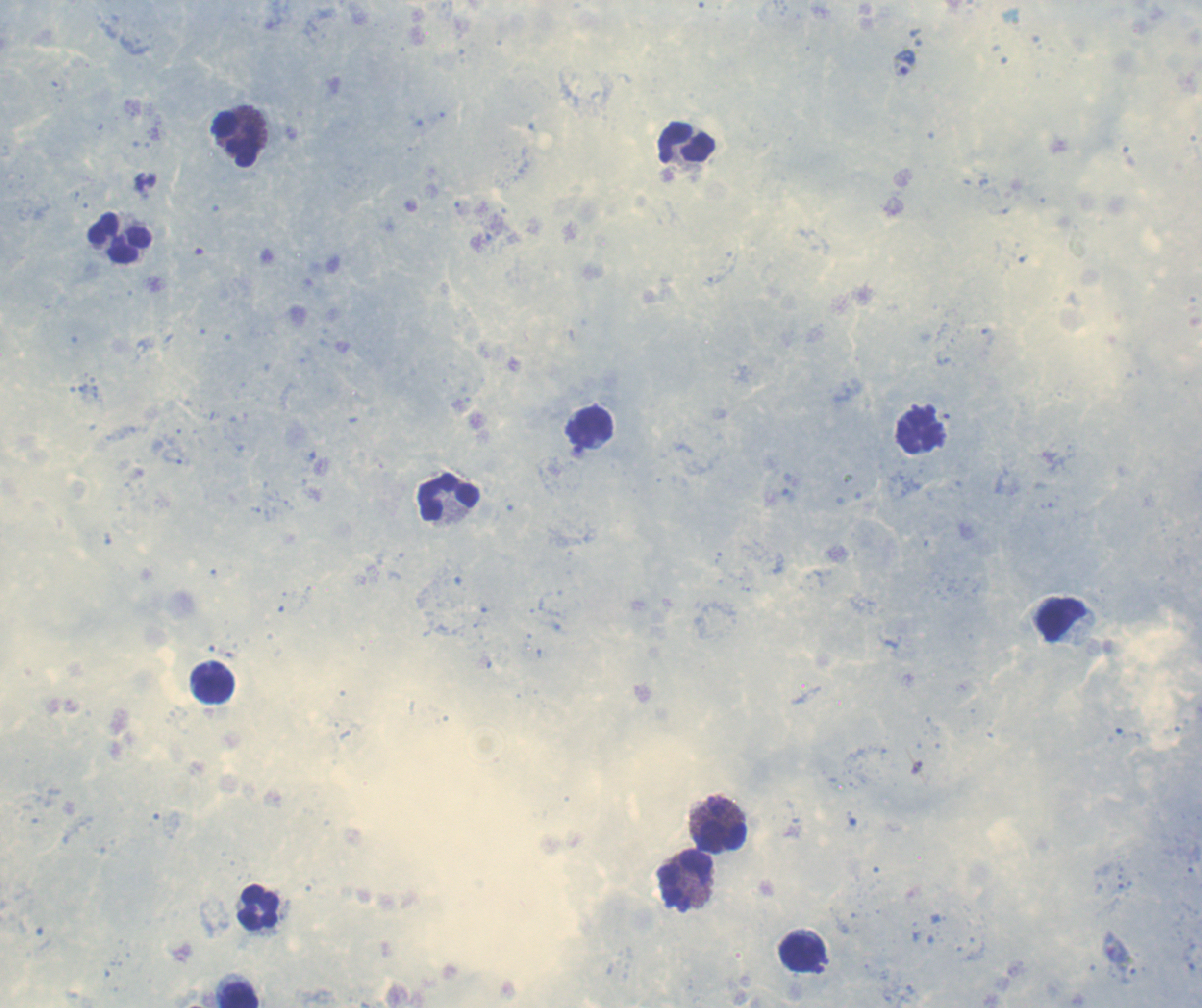
Approximate object centers, in pixels from the top-left corner. Trophozoite locations: (x=905, y=62). Leukocyte locations: (x=235, y=139), (x=686, y=143), (x=120, y=239), (x=592, y=428), (x=921, y=431), (x=449, y=498), (x=1062, y=620), (x=216, y=687), (x=722, y=823), (x=686, y=881), (x=259, y=908), (x=800, y=953), (x=239, y=995). Romanowsky-stained preparation. 100x magnification. Single field of view. Image is 1202×1008 pixels. Previously used in an actual diagnosis. Coloration quality: good. Result: positive for Plasmodium parasites. Thick blood film. Background quality: satisfactory.